Identify the parasite.
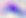
This is Toxoplasma gondii.

magnification = 400x
modality = micrograph